Name the parasite shown.
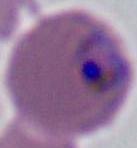

This is Plasmodium.

Summary:
  - Modality: micrograph
  - Magnification: 400x or 1000x